Locate and identify every blood parasite.
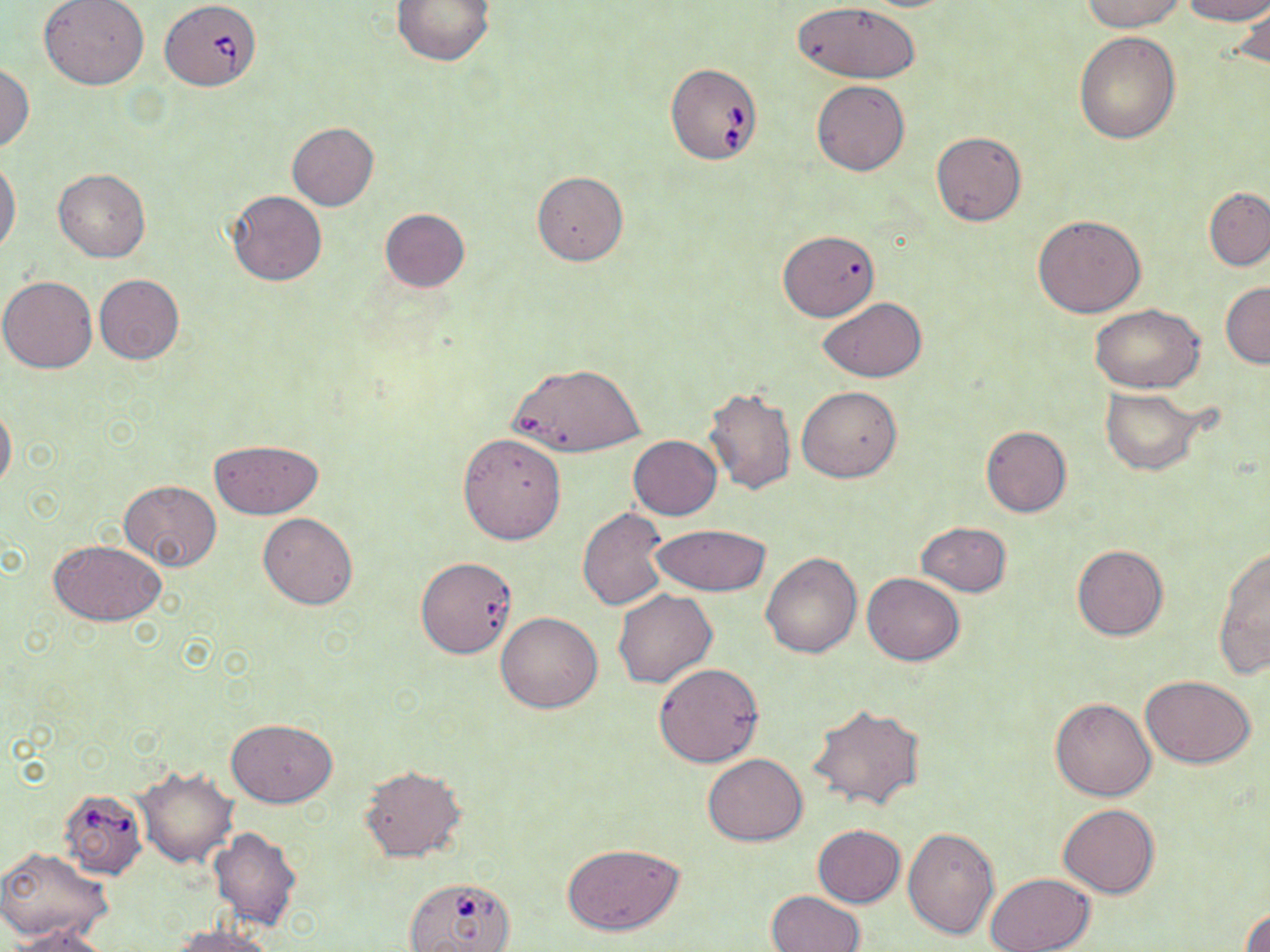

Approximate bounding boxes as (x1,y1)-(x2,y2) corner pairs in pixels.
Babesia divergens-infected red blood cells: (160,0)-(261,90), (665,63)-(763,165), (510,362)-(644,457), (58,787)-(146,879), (399,880)-(511,952).
No Plasmodium falciparum, Plasmodium ovale, Plasmodium malariae, Plasmodium vivax, or Trypanosoma brucei observed.

Summary:
  - Uninfected red blood cell locations: (38,0)-(151,89), (391,0)-(496,65), (1078,0)-(1184,30), (1180,0)-(1270,24), (792,2)-(922,86), (1230,5)-(1270,74), (1074,31)-(1182,144), (0,63)-(34,152), (811,79)-(910,176), (287,122)-(379,210), (931,131)-(1027,226), (0,158)-(22,253), (53,168)-(150,262), (532,171)-(628,265), (1204,187)-(1270,271), (226,190)-(326,286), (378,209)-(470,292), (1033,214)-(1146,317), (778,230)-(880,321), (94,274)-(184,364), (1,275)-(98,373), (1221,281)-(1270,367), (817,297)-(926,382), (1091,302)-(1206,392), (799,386)-(902,481), (702,387)-(797,495), (1100,388)-(1208,475), (0,402)-(16,491), (981,426)-(1071,517), (458,433)-(566,543), (627,436)-(722,520), (209,439)-(323,518), (118,480)-(223,571), (577,508)-(668,610), (258,513)-(358,609), (917,521)-(1013,596), (650,523)-(771,597), (49,540)-(165,626), (1072,544)-(1168,640), (1214,545)-(1270,676), (761,552)-(862,659), (416,556)-(517,659), (861,572)-(964,665), (612,588)-(718,688), (495,611)-(603,713), (653,663)-(763,767), (1140,675)-(1257,769), (1050,697)-(1157,801), (807,703)-(925,811), (226,719)-(337,807), (703,752)-(808,846), (358,764)-(465,862), (135,767)-(238,868), (1058,805)-(1159,899), (813,825)-(905,908), (903,826)-(999,940), (209,827)-(302,930), (561,843)-(687,935), (0,846)-(112,943), (984,872)-(1095,952), (767,890)-(865,952), (1241,907)-(1270,952), (169,922)-(281,951), (12,923)-(114,951)
  - Slide-level diagnosis: Babesia divergens
  - Image size: 1270×952 pixels
  - Magnification: 1000x
  - Stain: May-Grünwald-Giemsa
  - Modality: light microscopy
  - Preparation: thin blood smear
  - Field of view: single